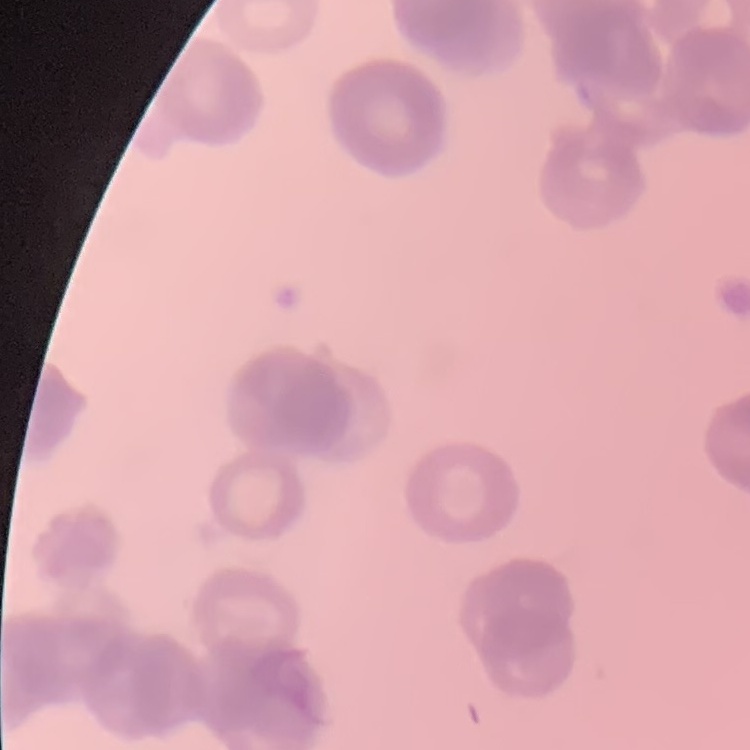

Summary:
  - Erythrocyte morphology: rouleaux formation
  - Image type: square crop of a larger photomicrograph
  - Stain: Field's or Giemsa
  - Preparation: thin blood smear